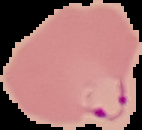

image type = segmented cell region with the area outside set to black
result = Plasmodium parasites identified
image size = 142×130 pixels
preparation = thin blood smear